Point out each malaria parasite.
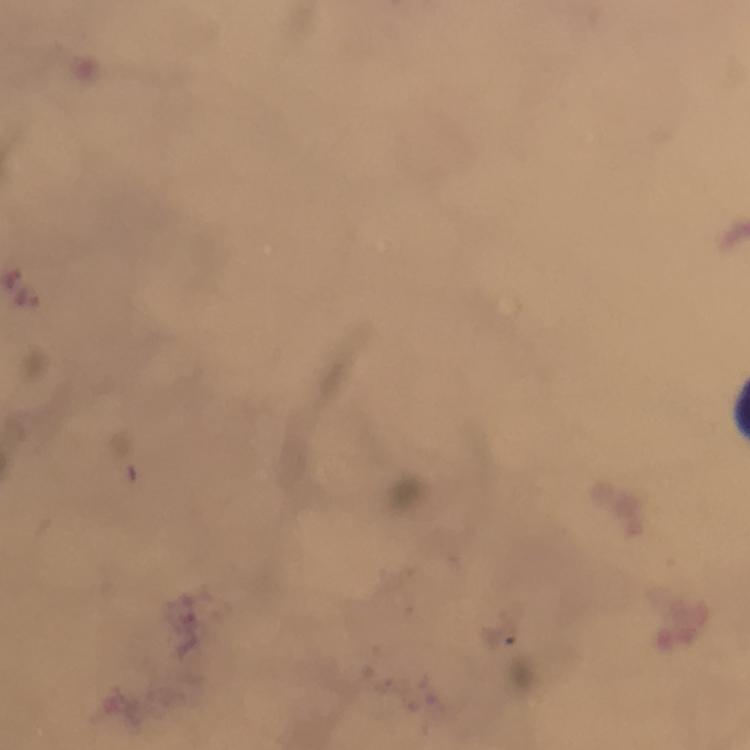

Approximate centers as [x, y] in pixels.
Malaria parasites: [29, 296].

Summary:
  - Preparation: thick smear
  - Image size: 750×750 pixels
  - Cropped from: a single field of view
  - Context: from a malaria diagnostic workup
  - Capture: smartphone photograph through a microscope
  - Immersion oil: applied
  - Magnification: 100x
  - Stain: Giemsa